Classify this cell by malaria status.
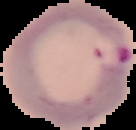
It is parasitized.

{
  "image_type": "segmented cell region on a black background",
  "image_size": "136×130 pixels",
  "preparation": "thin blood smear"
}